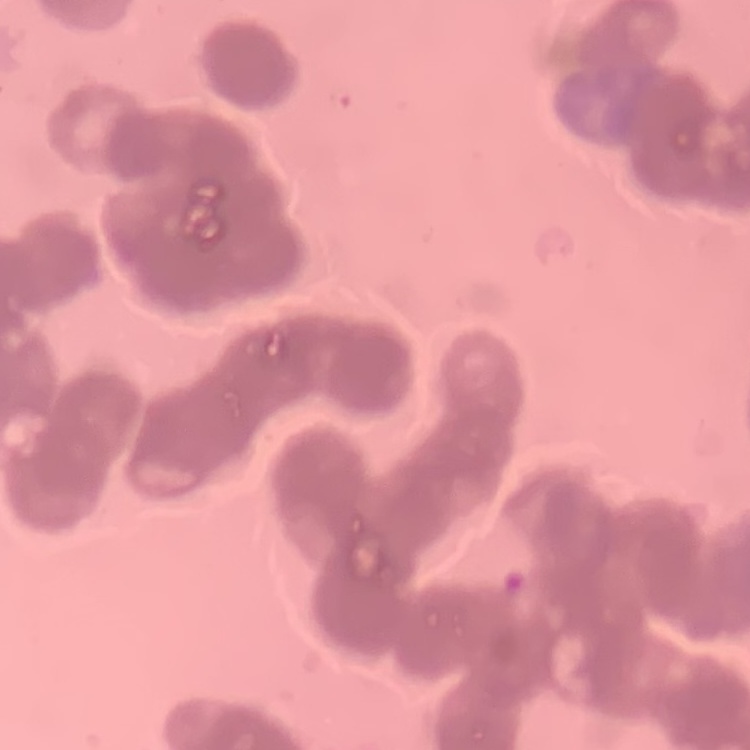
{
  "erythrocyte_morphology": "rouleaux formation",
  "stain": "Field's or Giemsa",
  "preparation": "thin blood smear",
  "image_type": "square crop of a larger photomicrograph"
}